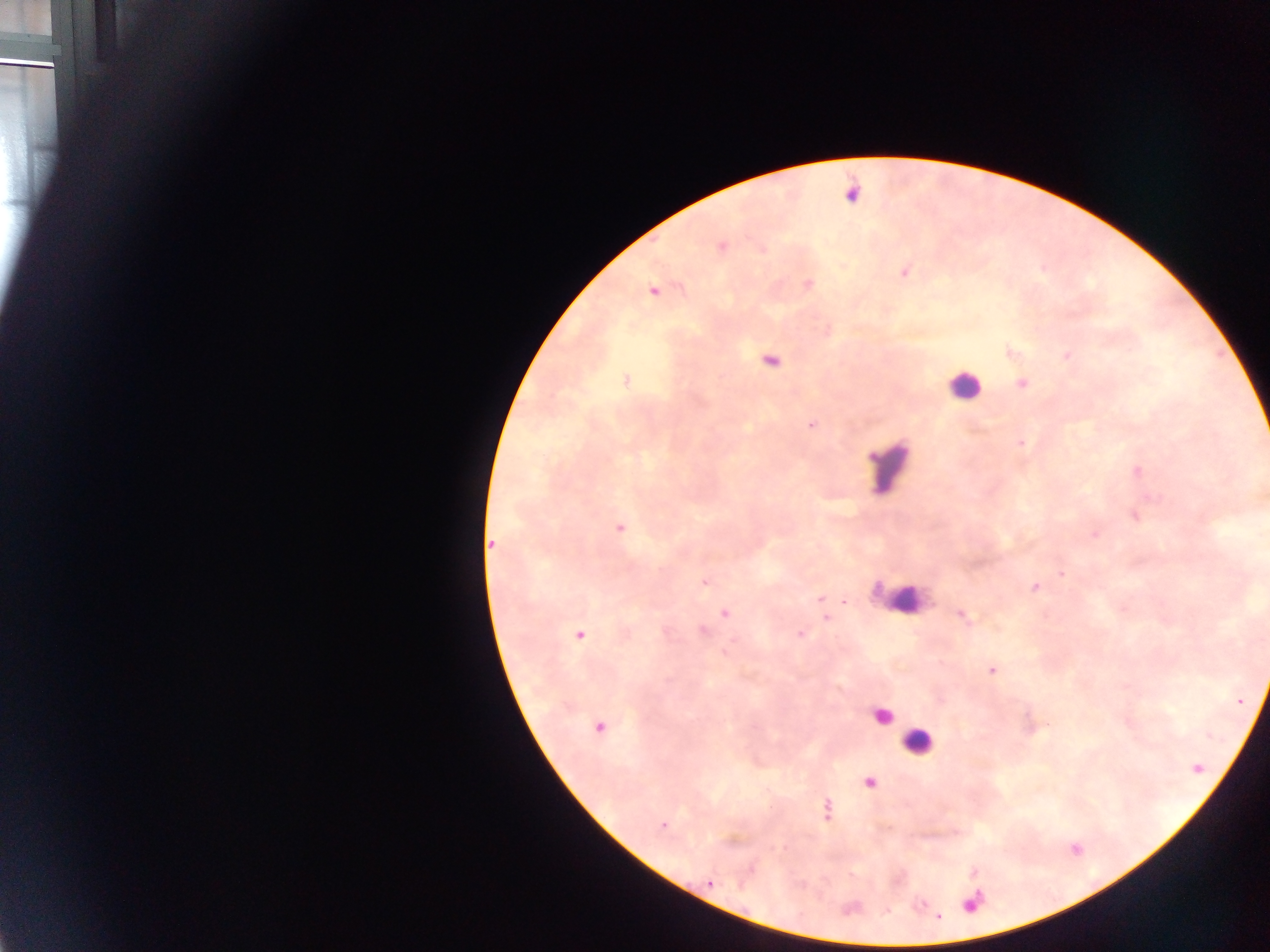

Approximate centers as (x, y) in pixels. Leukocyte locations: (957, 392), (891, 459), (884, 717), (917, 746). Malaria parasite locations: (852, 193), (722, 248), (761, 249), (904, 273), (807, 282), (1008, 351), (1067, 356), (770, 359), (625, 379), (1021, 383), (811, 423), (1020, 442), (870, 456), (1135, 469), (1134, 515), (620, 527), (1094, 531), (493, 544), (1061, 574), (705, 580), (1033, 586), (875, 592), (819, 596), (908, 599), (899, 600), (844, 601), (1123, 608), (724, 612), (959, 614), (827, 618), (704, 631), (799, 633), (579, 635), (728, 647), (991, 671), (668, 678), (599, 726), (869, 782), (828, 810), (708, 884), (971, 906), (885, 910), (940, 918). Collected in Ghana. Single field of view. Mobile-phone photograph taken through the microscope. Image is 1270×952 pixels. Thick blood smear.